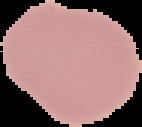
Summary:
  - Image size: 142×127 pixels
  - Image type: segmented cell region with the area outside set to black
  - Result: negative for malaria parasites
  - Preparation: thin blood film